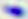
magnification = 400x
identification = Toxoplasma gondii
modality = photomicrograph